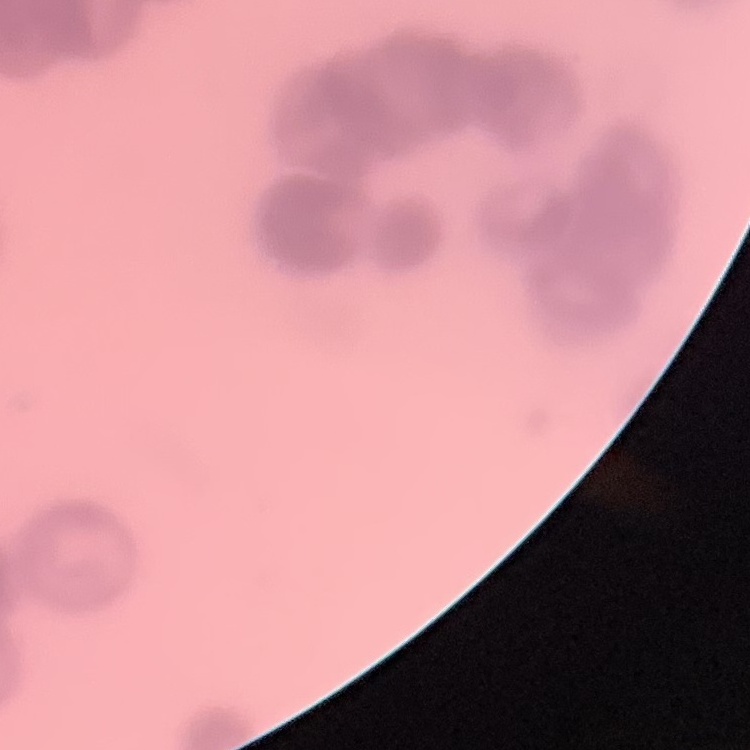
erythrocyte morphology = rouleaux formation
image type = square crop of a larger photomicrograph
stain = Field's or Giemsa
preparation = thin blood film